Give the position of every leukocyte visible.
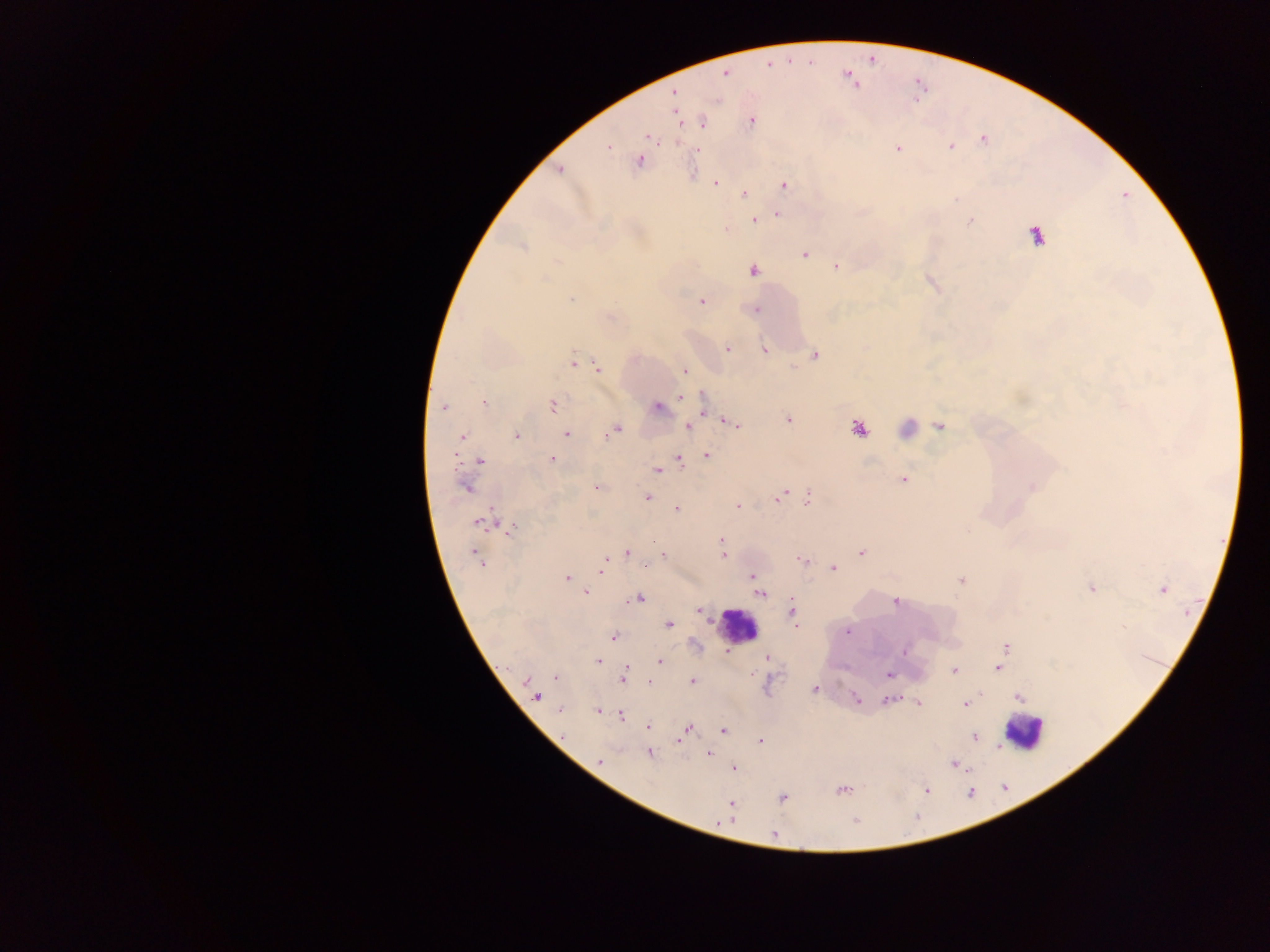

Approximate centers as x y in pixels.
Leukocytes: 904 429; 739 627; 1023 731.

Summary:
  - Malaria parasite locations: 767 64; 725 73; 847 77; 672 92; 677 116; 750 120; 701 122; 649 138; 982 138; 677 141; 607 146; 950 147; 898 148; 697 150; 640 160; 559 169; 692 173; 715 184; 782 186; 743 193; 777 213; 754 219; 970 220; 727 229; 1035 234; 523 247; 804 254; 836 266; 752 270; 572 298; 701 301; 757 310; 727 348; 765 350; 813 354; 574 361; 597 367; 684 371; 680 397; 484 402; 552 405; 443 407; 656 407; 703 411; 788 419; 728 421; 735 424; 687 426; 939 426; 857 429; 614 430; 566 434; 517 435; 462 437; 705 454; 551 458; 679 460; 479 461; 656 470; 902 479; 466 487; 596 487; 1032 487; 782 494; 647 497; 808 498; 738 506; 677 509; 482 521; 508 529; 721 539; 627 552; 861 552; 663 554; 723 555; 478 559; 801 559; 649 562; 603 563; 646 565; 832 568; 602 570; 751 575; 566 578; 962 580; 756 585; 1090 587; 1162 589; 585 592; 760 593; 636 598; 895 601; 698 610; 792 611; 668 624; 846 630; 613 636; 1006 646; 903 652; 727 653; 724 654; 766 657; 597 660; 660 661; 997 667; 954 670; 888 675; 555 676; 623 676; 692 681; 529 682; 649 682; 814 689; 536 695; 1019 696; 888 699; 856 700; 917 702; 965 704; 559 709; 597 710; 619 714; 648 725; 687 729; 723 730; 974 736; 679 740; 758 741; 997 747; 648 753; 709 754; 600 761; 954 764; 733 767; 841 790; 925 790; 782 798; 731 805; 727 819; 773 835
  - Image size: 1270×952 pixels
  - Field of view: single
  - Country: Ghana
  - Preparation: thick blood film
  - Capture: mobile-phone photograph through a microscope